Point out each Plasmodium parasite.
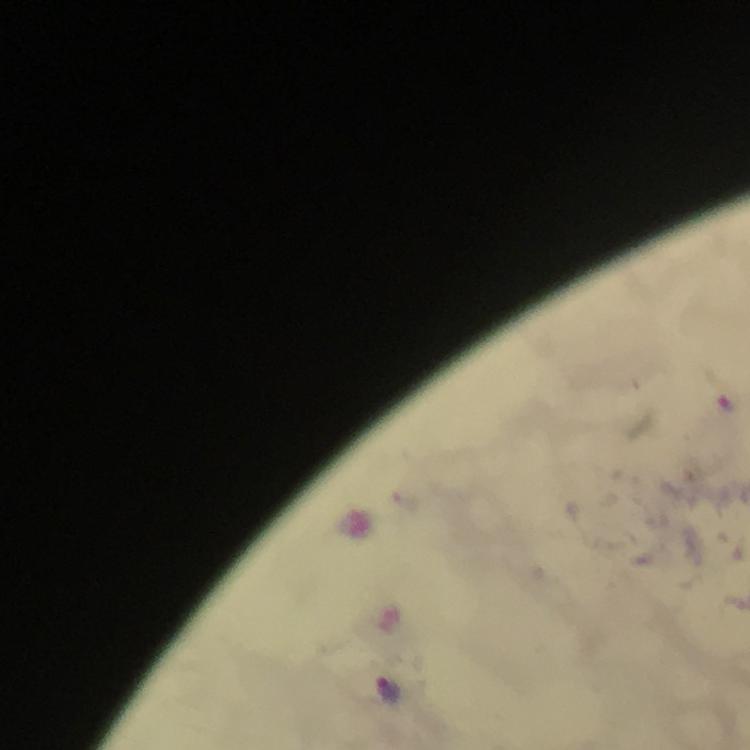
Approximate centers as {x, y} in pixels.
Plasmodium parasites: {388, 692}.

Summary:
  - Stain: Giemsa
  - Magnification: 100x
  - Immersion oil: used
  - Cropped from: one field of view
  - Context: from a malaria diagnostic workup
  - Image size: 750×750 pixels
  - Preparation: thick smear
  - Capture: smartphone camera through the microscope